Report the malaria status of this cell.
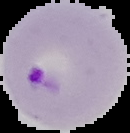
Parasitized.

Summary:
  - Preparation: thin blood smear
  - Image type: cell region segmented out of the field of view; surrounding area masked to black
  - Image size: 130×133 pixels